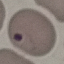
Malaria status: uninfected. Cell patch, automatically extracted from a larger field of view and resized to 64 × 64 pixels. Giemsa-stained preparation. Thin blood film. Acquired by smartphone through the microscope eyepiece.